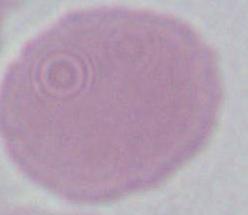
modality = micrograph
identification = red blood cell
magnification = 1000x